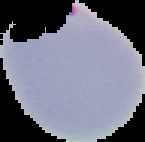

Summary:
  - Image type: cell region segmented out of the field of view; surrounding area masked to black
  - Preparation: thin blood film
  - Result: malaria parasites detected
  - Image size: 145×142 pixels